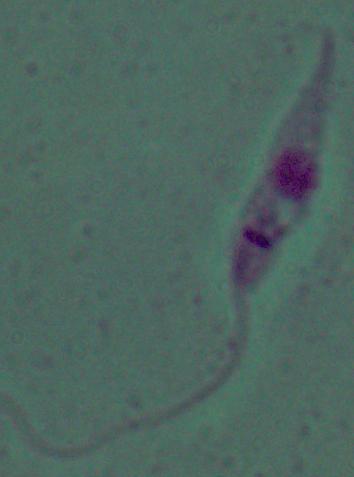
modality = micrograph
identification = Leishmania
magnification = 1000x